Name the cell type shown.
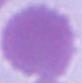

This is an erythrocyte.

1000x magnification. Photomicrograph.